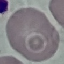

result = no malaria parasites detected
capture = smartphone camera at the microscope eyepiece
stain = Giemsa
preparation = thin smear
image type = automatically extracted cell patch, resized to 64 × 64 pixels